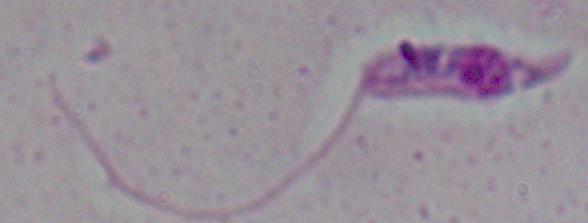
A Leishmania parasite is shown. Captured at 1000x magnification. Micrograph.